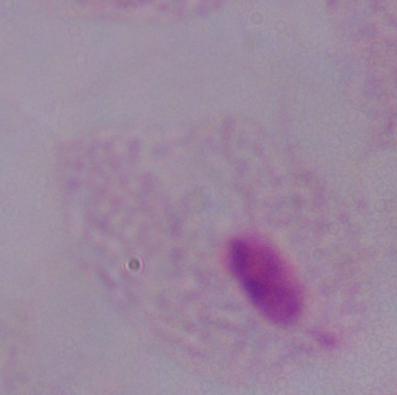

Captured at 1000x magnification. A trichomonad is shown. Photomicrograph.